Report the malaria status of this cell.
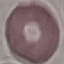
Uninfected.

capture: smartphone through the microscope eyepiece
image_type: automatically extracted cell patch, resized to 64 × 64 pixels
preparation: thin smear
stain: Giemsa